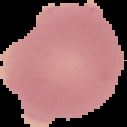

Summary:
  - Image size: 127×127 pixels
  - Result: no Plasmodium parasites detected
  - Preparation: thin blood smear
  - Image type: segmented cell region on a black background